Comment on the morphology of the red blood cells.
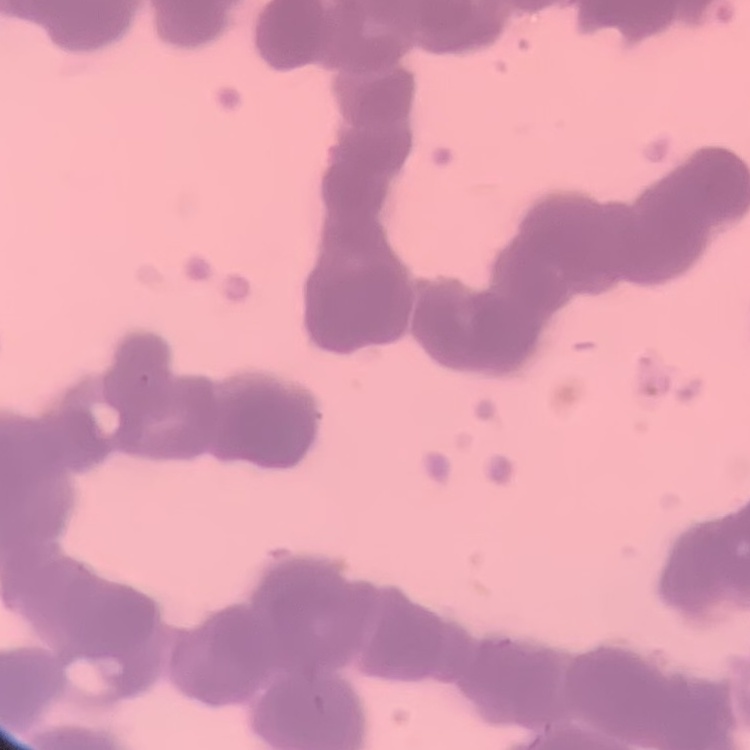
They show rouleaux formation.

Summary:
  - Image type: square crop of a larger photomicrograph
  - Preparation: thin blood smear
  - Stain: Field's or Giemsa